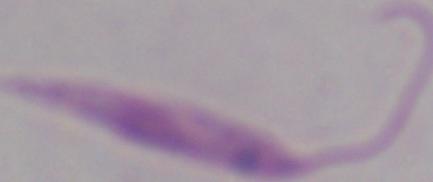 Micrograph. Captured at 1000x magnification. A Leishmania parasite is seen.